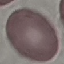

Summary:
  - Result: no malaria parasites detected
  - Capture: smartphone camera at the microscope eyepiece
  - Preparation: thin blood smear
  - Image type: cell patch, automatically extracted from a larger field of view and resized to 64 × 64 pixels
  - Stain: Giemsa